Classify this cell by malaria status.
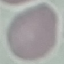

It is uninfected.

Acquired by smartphone through the microscope eyepiece. Giemsa stain. Cell patch, automatically extracted from a larger field of view and resized to 64 × 64 pixels. Thin blood film.